Give the position of every malaria parasite.
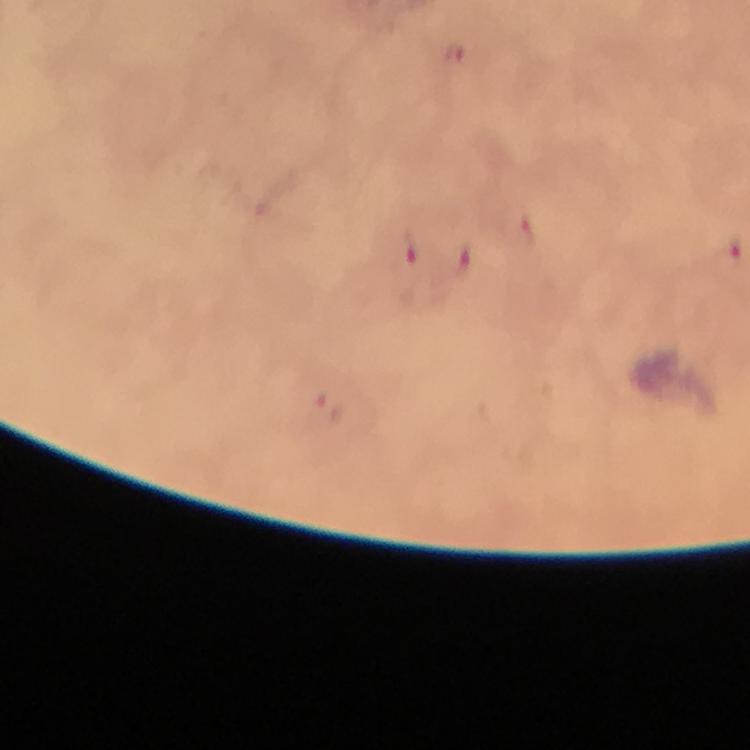
Approximate centers as (x, y) in pixels.
Malaria parasites: (456, 54), (521, 233), (410, 251), (728, 254), (461, 262).

Giemsa stain. 100x magnification. Cropped region of a single field of view. Immersion oil was used. Thick blood smear. Image is 750×750 pixels. From a diagnostic examination for malaria. Smartphone photograph taken through a microscope.